Outline platelets.
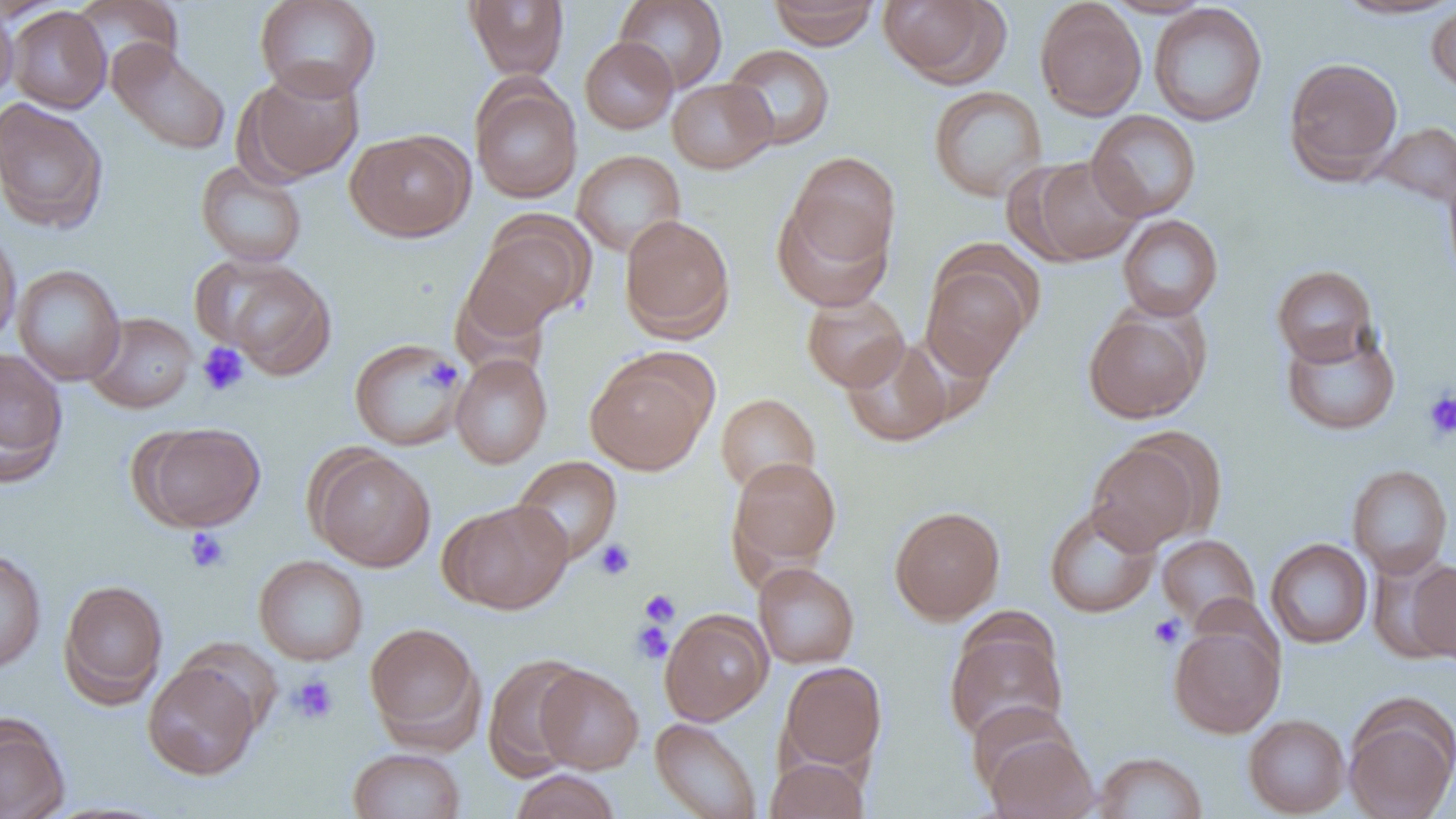

Approximate bounding boxes as (x1,y1)-(x2,y2) corner pairs in pixels.
Platelets: (197,342)-(250,397), (421,353)-(462,396), (1422,389)-(1456,441), (185,527)-(230,573), (594,540)-(636,581), (639,589)-(681,627), (1149,614)-(1185,649), (631,621)-(673,664), (289,674)-(339,725).

Summary:
  - Uninfected red blood cell locations: (71,0)-(186,81), (254,0)-(381,101), (464,0)-(570,79), (614,0)-(728,93), (768,0)-(880,49), (878,0)-(1008,87), (1102,0)-(1214,18), (1333,0)-(1455,20), (1034,1)-(1146,121), (1148,3)-(1268,127), (1426,3)-(1456,94), (0,4)-(19,109), (6,6)-(111,113), (580,37)-(678,134), (107,41)-(231,155), (723,44)-(836,150), (1283,56)-(1403,183), (241,64)-(366,184), (667,78)-(777,173), (470,79)-(582,202), (928,85)-(1047,201), (0,98)-(109,234), (1086,110)-(1201,221), (1372,121)-(1456,208), (346,130)-(475,242), (572,149)-(686,256), (787,151)-(900,268), (1021,156)-(1144,265), (196,160)-(307,267), (1442,162)-(1456,288), (772,199)-(891,311), (619,214)-(735,341), (1117,215)-(1223,321), (464,221)-(590,339), (0,228)-(21,350), (195,256)-(337,378), (921,258)-(1034,381), (12,265)-(125,385), (1272,265)-(1378,366), (801,292)-(910,392), (1083,309)-(1207,423), (85,312)-(198,413), (1280,323)-(1401,436), (840,336)-(955,447), (349,337)-(467,451), (0,347)-(68,485), (450,353)-(553,469), (586,356)-(712,475), (716,393)-(820,495), (135,421)-(265,531), (1086,439)-(1206,554), (309,449)-(436,571), (512,456)-(622,564), (728,456)-(841,573), (1347,464)-(1453,579), (442,499)-(574,614), (1044,503)-(1161,618), (889,505)-(1005,624), (1157,534)-(1260,630), (1265,538)-(1373,649), (0,547)-(47,674), (253,554)-(368,665), (1406,558)-(1456,664), (753,562)-(859,669), (58,579)-(169,706), (659,610)-(773,725), (944,620)-(1068,746), (364,621)-(485,747), (1168,621)-(1285,738), (482,653)-(590,780), (143,661)-(262,781), (778,661)-(887,775), (536,665)-(644,773), (966,700)-(1077,798), (1343,701)-(1456,819), (0,714)-(69,819), (1243,714)-(1350,817), (650,718)-(762,819), (981,728)-(1098,819), (348,748)-(466,819), (1093,752)-(1208,818), (764,756)-(870,819), (508,770)-(621,819)
  - Slide-level diagnosis: negative for blood parasites
  - Modality: optical microscopy
  - Field of view: single
  - Image size: 1456×819 pixels
  - Magnification: 1000x
  - Preparation: thin blood film